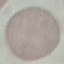
{
  "malaria_status": "uninfected",
  "preparation": "thin blood smear",
  "capture": "smartphone camera at the microscope eyepiece",
  "image_type": "automatically extracted cell patch, resized to 64 × 64 pixels",
  "stain": "Giemsa"
}